State which parasite is depicted.
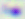
This is Toxoplasma gondii.

Micrograph. Captured at 400x magnification.